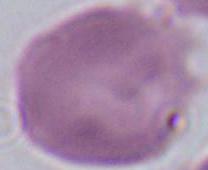

Photomicrograph. An erythrocyte is shown. 1000x magnification.